Locate and identify every blood parasite.
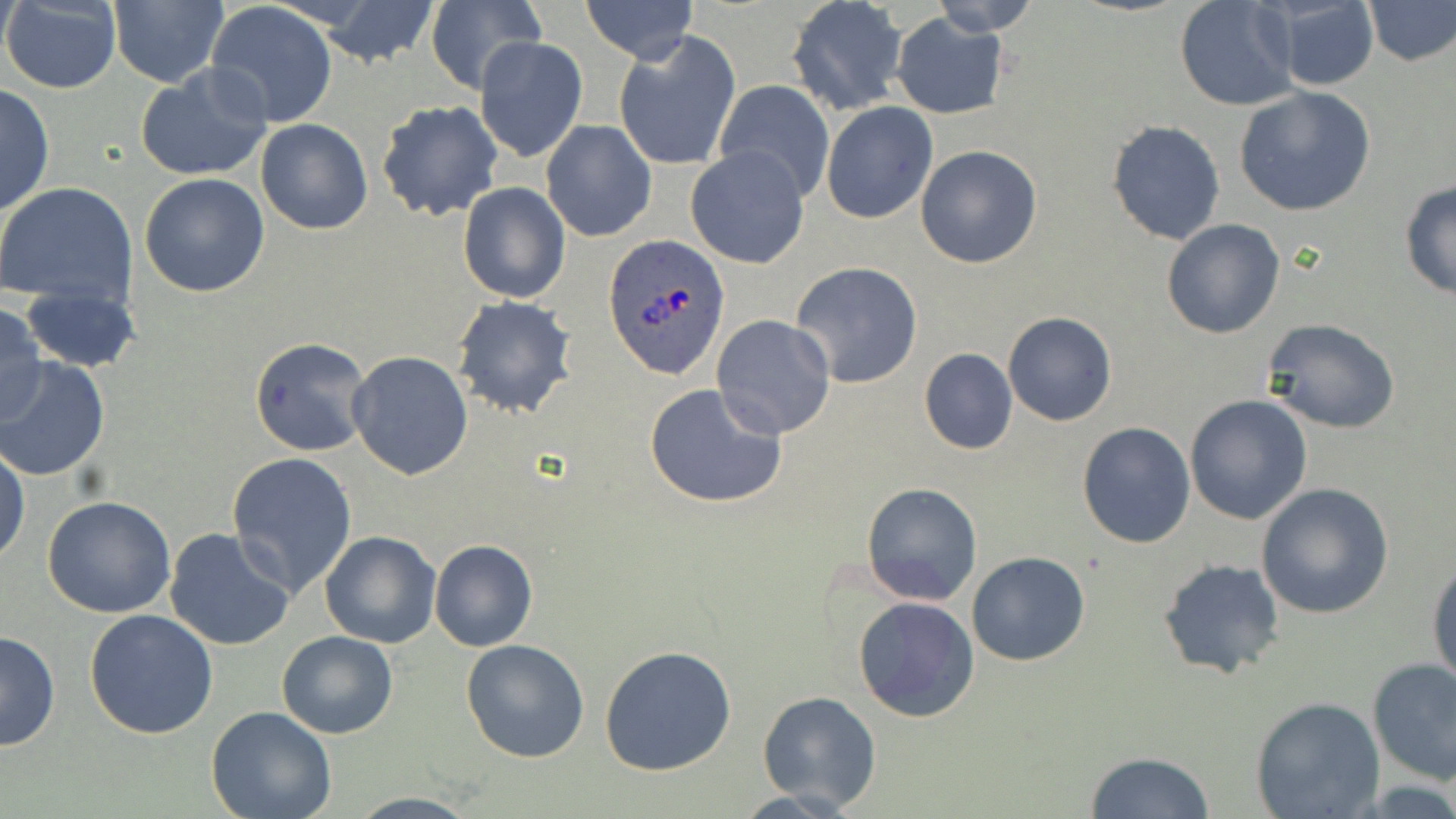
Approximate bounding boxes as named x1/y1/x2/y2 corners in pixels.
Plasmodium ovale-infected red blood cells: (x1=600, y1=236, x2=729, y2=380).
No Plasmodium falciparum, Plasmodium malariae, Plasmodium vivax, Babesia divergens, or Trypanosoma brucei observed.

slide-level diagnosis = Plasmodium ovale
image size = 1456×819 pixels
modality = optical microscopy
stain = May-Grünwald-Giemsa
magnification = 1000x
preparation = thin blood film
uninfected red blood cell locations = approximate bounding boxes as named x1/y1/x2/y2 corners in pixels: (x1=317, y1=0, x2=437, y2=66), (x1=581, y1=0, x2=698, y2=62), (x1=927, y1=0, x2=1040, y2=36), (x1=1175, y1=0, x2=1298, y2=112), (x1=1268, y1=0, x2=1380, y2=90), (x1=1, y1=1, x2=122, y2=93), (x1=107, y1=1, x2=229, y2=87), (x1=1365, y1=1, x2=1455, y2=66), (x1=206, y1=2, x2=337, y2=127), (x1=786, y1=2, x2=906, y2=116), (x1=422, y1=3, x2=542, y2=94), (x1=891, y1=14, x2=1007, y2=119), (x1=614, y1=33, x2=741, y2=172), (x1=474, y1=37, x2=587, y2=164), (x1=135, y1=65, x2=273, y2=182), (x1=713, y1=80, x2=834, y2=202), (x1=0, y1=82, x2=54, y2=218), (x1=1232, y1=86, x2=1377, y2=217), (x1=376, y1=101, x2=504, y2=222), (x1=821, y1=101, x2=937, y2=224), (x1=1107, y1=118, x2=1225, y2=245), (x1=255, y1=119, x2=373, y2=235), (x1=540, y1=120, x2=658, y2=242), (x1=915, y1=145, x2=1042, y2=269), (x1=686, y1=147, x2=810, y2=270), (x1=140, y1=172, x2=271, y2=297), (x1=1399, y1=179, x2=1456, y2=299), (x1=0, y1=182, x2=138, y2=308), (x1=458, y1=182, x2=571, y2=304), (x1=1161, y1=218, x2=1286, y2=339), (x1=792, y1=262, x2=924, y2=388), (x1=20, y1=287, x2=141, y2=372), (x1=451, y1=295, x2=578, y2=420), (x1=0, y1=302, x2=49, y2=427), (x1=1003, y1=312, x2=1117, y2=427), (x1=711, y1=313, x2=836, y2=438), (x1=1262, y1=318, x2=1400, y2=433), (x1=250, y1=338, x2=373, y2=456), (x1=919, y1=348, x2=1017, y2=455), (x1=346, y1=351, x2=475, y2=481), (x1=0, y1=358, x2=111, y2=482), (x1=644, y1=383, x2=788, y2=509), (x1=1185, y1=396, x2=1313, y2=524), (x1=1077, y1=422, x2=1197, y2=549), (x1=1, y1=443, x2=27, y2=564), (x1=226, y1=452, x2=358, y2=598), (x1=861, y1=482, x2=983, y2=605), (x1=1255, y1=482, x2=1394, y2=618), (x1=42, y1=494, x2=177, y2=618), (x1=164, y1=527, x2=295, y2=653), (x1=319, y1=531, x2=440, y2=648), (x1=428, y1=539, x2=539, y2=652), (x1=966, y1=552, x2=1091, y2=665), (x1=1157, y1=558, x2=1287, y2=681), (x1=1428, y1=558, x2=1456, y2=692), (x1=852, y1=596, x2=981, y2=723), (x1=84, y1=608, x2=218, y2=739), (x1=0, y1=629, x2=60, y2=753), (x1=278, y1=632, x2=397, y2=739), (x1=461, y1=639, x2=589, y2=762), (x1=600, y1=644, x2=737, y2=775), (x1=1367, y1=659, x2=1456, y2=788), (x1=756, y1=690, x2=881, y2=812), (x1=1249, y1=697, x2=1386, y2=819), (x1=207, y1=707, x2=337, y2=819), (x1=1084, y1=750, x2=1217, y2=819)
field of view = single